Comment on the morphology of the erythrocytes.
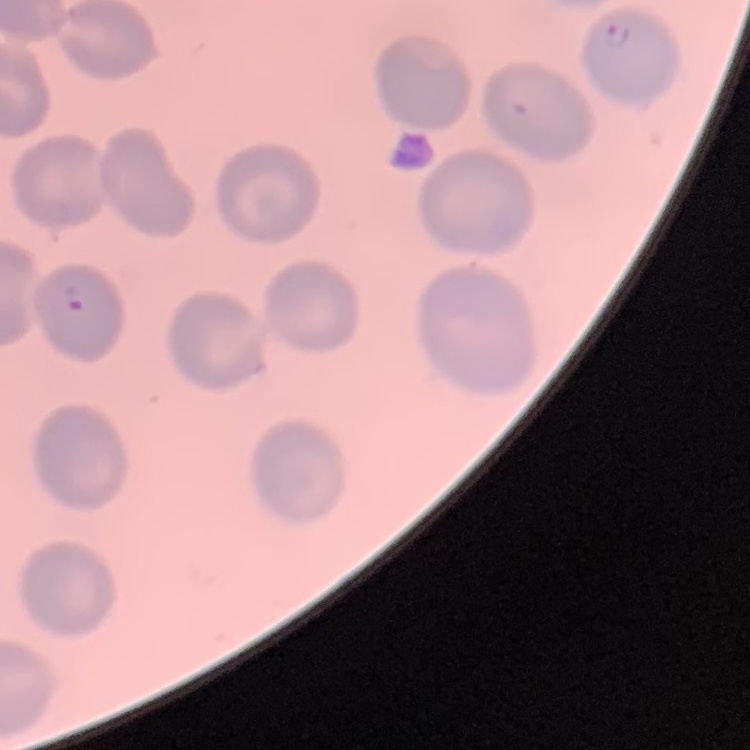
They show no rouleaux formation.

preparation = thin peripheral smear
image type = square crop of a larger photomicrograph
stain = Field's or Giemsa